Identify the blood parasite species.
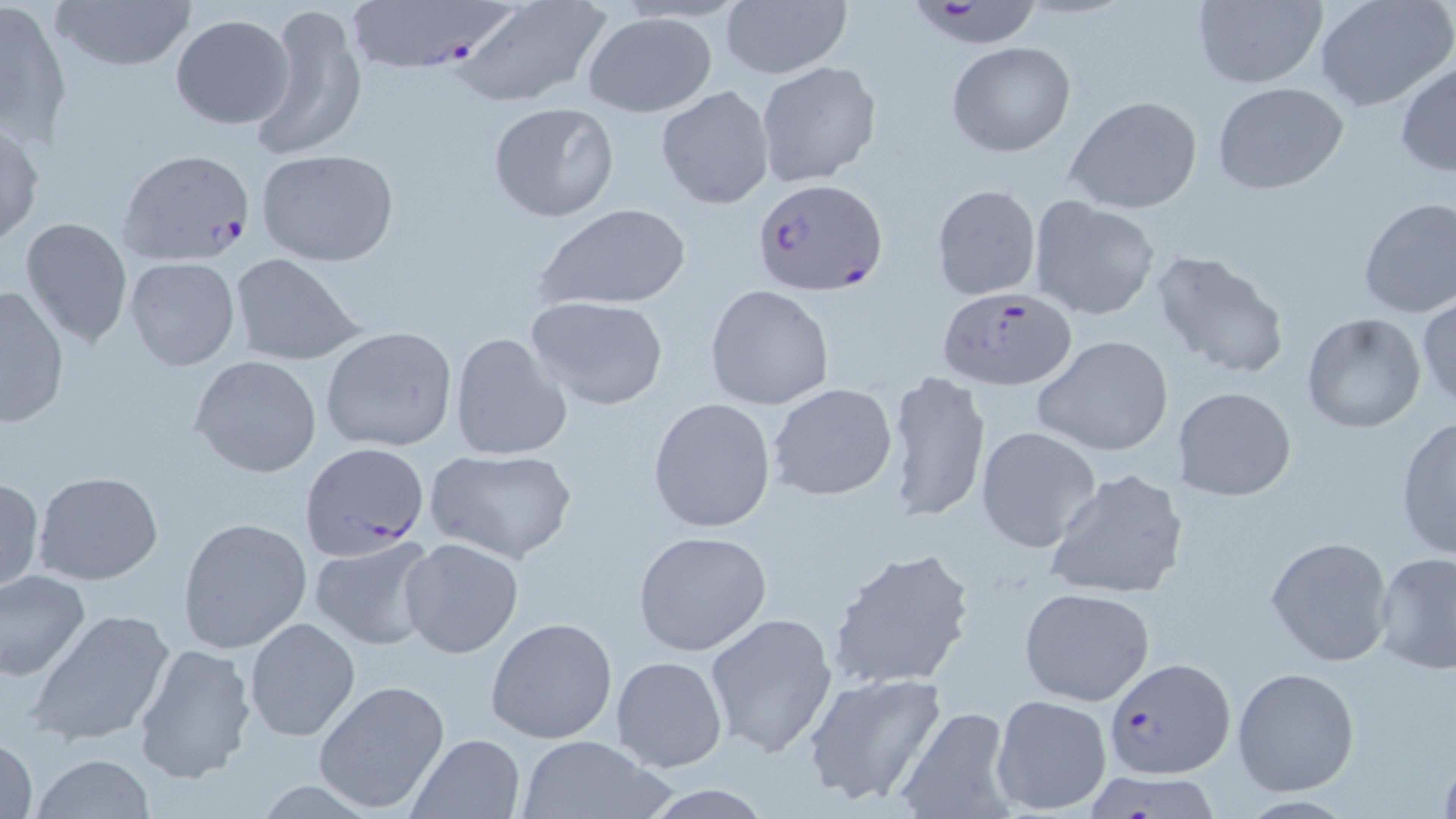

Plasmodium falciparum.

Approximate bounding boxes as (x1, y1, x2, y2) in pixels. Plasmodium falciparum-infected red blood cell locations: (343, 0, 512, 73), (916, 1, 1042, 50), (118, 146, 258, 268), (755, 178, 888, 298), (937, 285, 1077, 390), (301, 439, 432, 557), (1103, 654, 1232, 780). Uninfected red blood cell locations: (2, 0, 72, 142), (48, 0, 198, 75), (1190, 0, 1328, 89), (1313, 0, 1456, 114), (720, 2, 851, 80), (252, 3, 367, 162), (451, 3, 609, 109), (581, 11, 717, 117), (169, 14, 294, 130), (945, 41, 1076, 158), (756, 60, 881, 187), (1395, 61, 1456, 176), (1212, 82, 1350, 195), (657, 85, 775, 208), (1064, 95, 1204, 214), (486, 100, 620, 224), (0, 116, 44, 251), (255, 147, 399, 268), (931, 182, 1041, 301), (1028, 195, 1161, 321), (1356, 198, 1456, 318), (533, 203, 690, 314), (19, 217, 134, 349), (1150, 248, 1291, 382), (227, 252, 365, 366), (124, 255, 241, 370), (705, 284, 834, 411), (1, 285, 71, 427), (523, 294, 669, 412), (1417, 295, 1456, 411), (1300, 312, 1427, 434), (319, 325, 458, 454), (449, 332, 572, 461), (1033, 335, 1174, 458), (189, 355, 323, 478), (886, 369, 990, 524), (767, 381, 898, 501), (1172, 385, 1298, 502), (646, 396, 777, 532), (1395, 415, 1456, 562), (975, 425, 1103, 554), (425, 449, 579, 565), (1044, 466, 1188, 601), (33, 470, 164, 587), (0, 474, 44, 597), (178, 517, 312, 654), (632, 529, 772, 656), (308, 534, 438, 651), (1265, 535, 1395, 668), (400, 537, 524, 658), (826, 546, 977, 692), (1372, 551, 1456, 674), (0, 570, 92, 683), (1018, 587, 1155, 708), (25, 607, 178, 748), (704, 610, 839, 759), (244, 616, 361, 743), (486, 616, 618, 744), (132, 641, 259, 784), (609, 654, 728, 773), (1232, 666, 1361, 797), (802, 672, 945, 806), (314, 679, 451, 814), (990, 693, 1112, 816), (892, 706, 1017, 819), (0, 732, 39, 819), (407, 732, 524, 818), (515, 733, 668, 818), (30, 753, 156, 819), (1078, 772, 1228, 819). Optical microscopy. May-Grünwald-Giemsa-stained preparation. Thin blood smear. Single field of view. Captured at 1000x magnification. Image is 1456×819 pixels.